Report the malaria status of this cell.
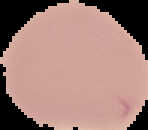

Uninfected.

Summary:
  - Preparation: thin blood smear
  - Image size: 148×130 pixels
  - Image type: segmented cell region with the area outside set to black